Give the preparation type.
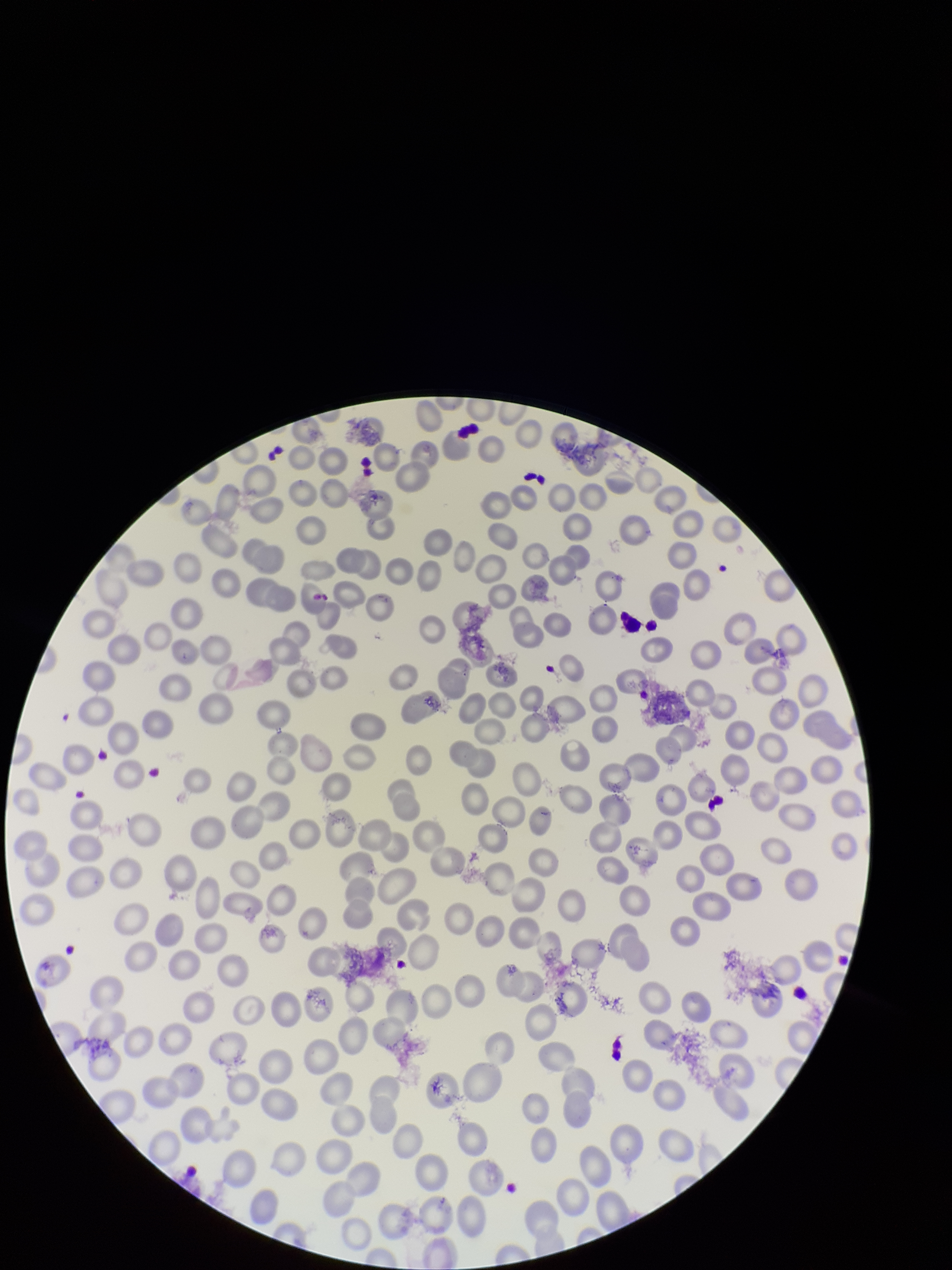
Thin.

parasitized red blood cell count = 0
parasitized red blood cells = none seen
patient malaria status = negative
red blood cell count = 247
image size = 952×1270 pixels
stain = Giemsa
capture = smartphone photograph through the microscope eyepiece
field of view = single